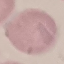
malaria status = uninfected
capture = smartphone camera at the microscope eyepiece
stain = Giemsa
image type = cell patch, automatically extracted from a larger field of view and resized to 64 × 64 pixels
preparation = thin smear